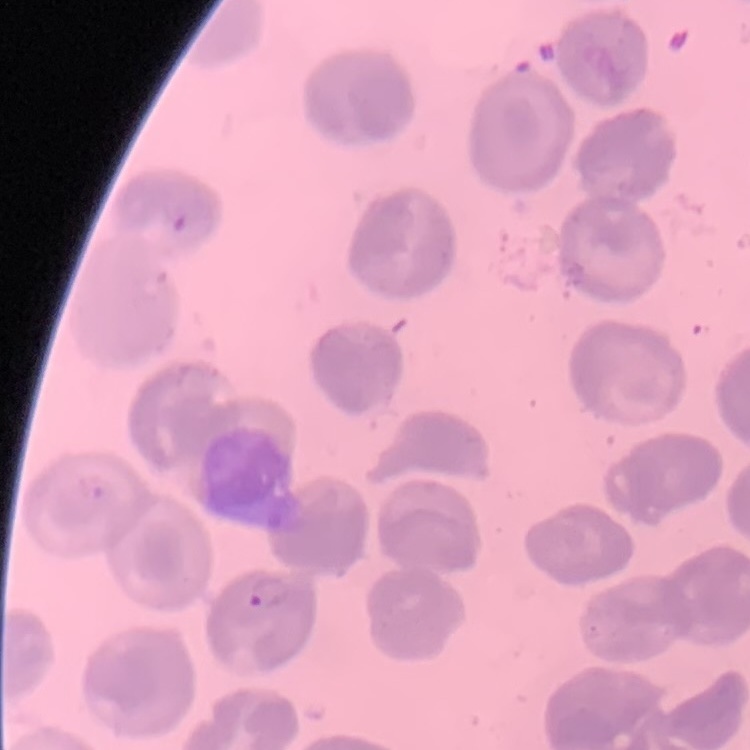 The erythrocytes exhibit no rouleaux formation. Stained with either Field's or Giemsa. Thin peripheral smear. Square crop of a larger photomicrograph.